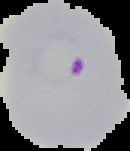

Image is 130×151 pixels. Malaria status: parasitized. Segmented cell region on a black background. From a thin blood film.